Locate every Plasmodium parasite.
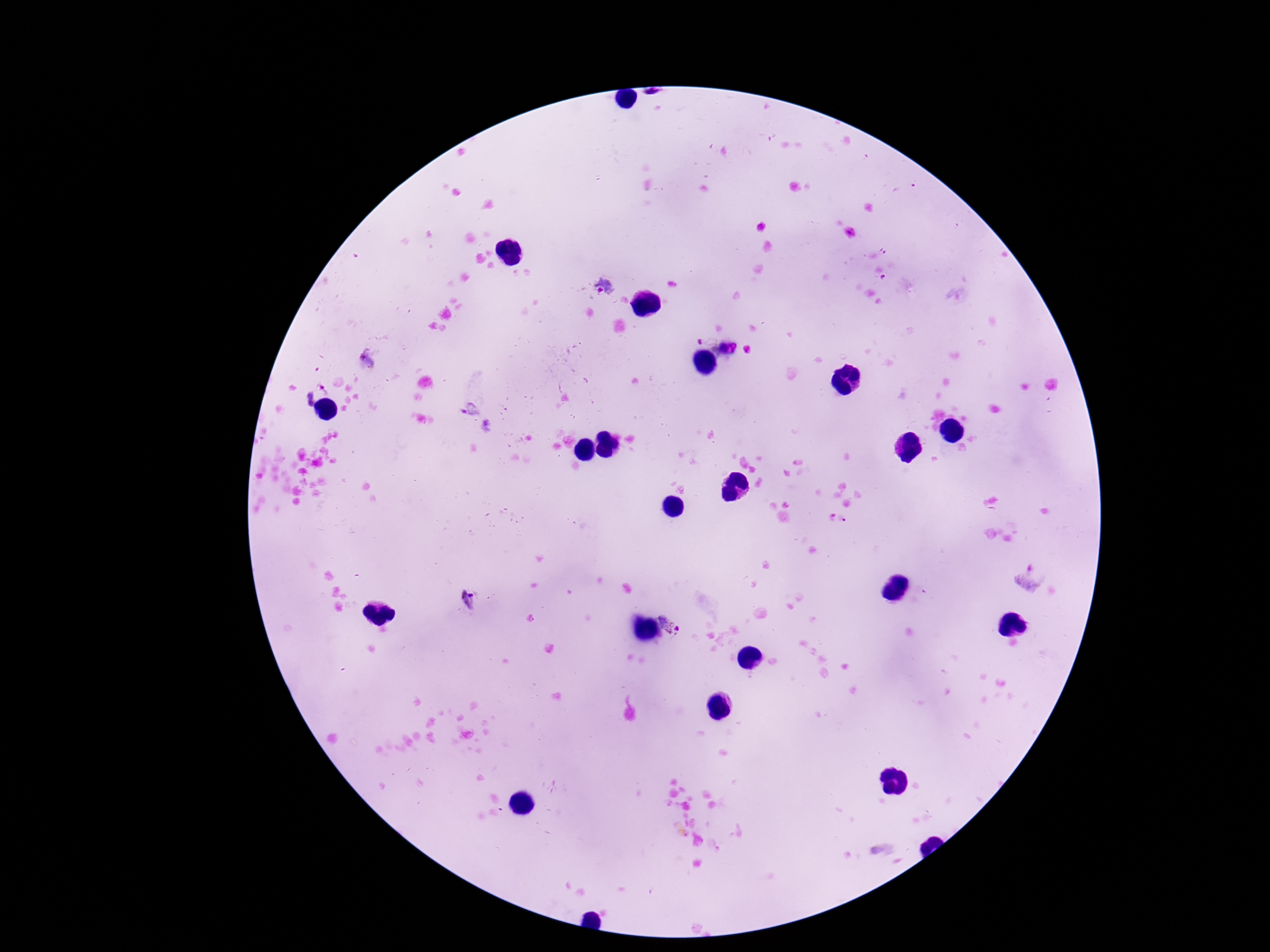
Approximate centers as {x, y} in pixels.
Plasmodium parasites: {608, 286}, {710, 335}, {312, 388}, {468, 599}, {675, 619}.

Giemsa stain. Thick blood film. Smartphone photograph taken through the microscope eyepiece. Patient malaria status: positive. One field from this slide. Image is 1270×952 pixels. 100x magnification.